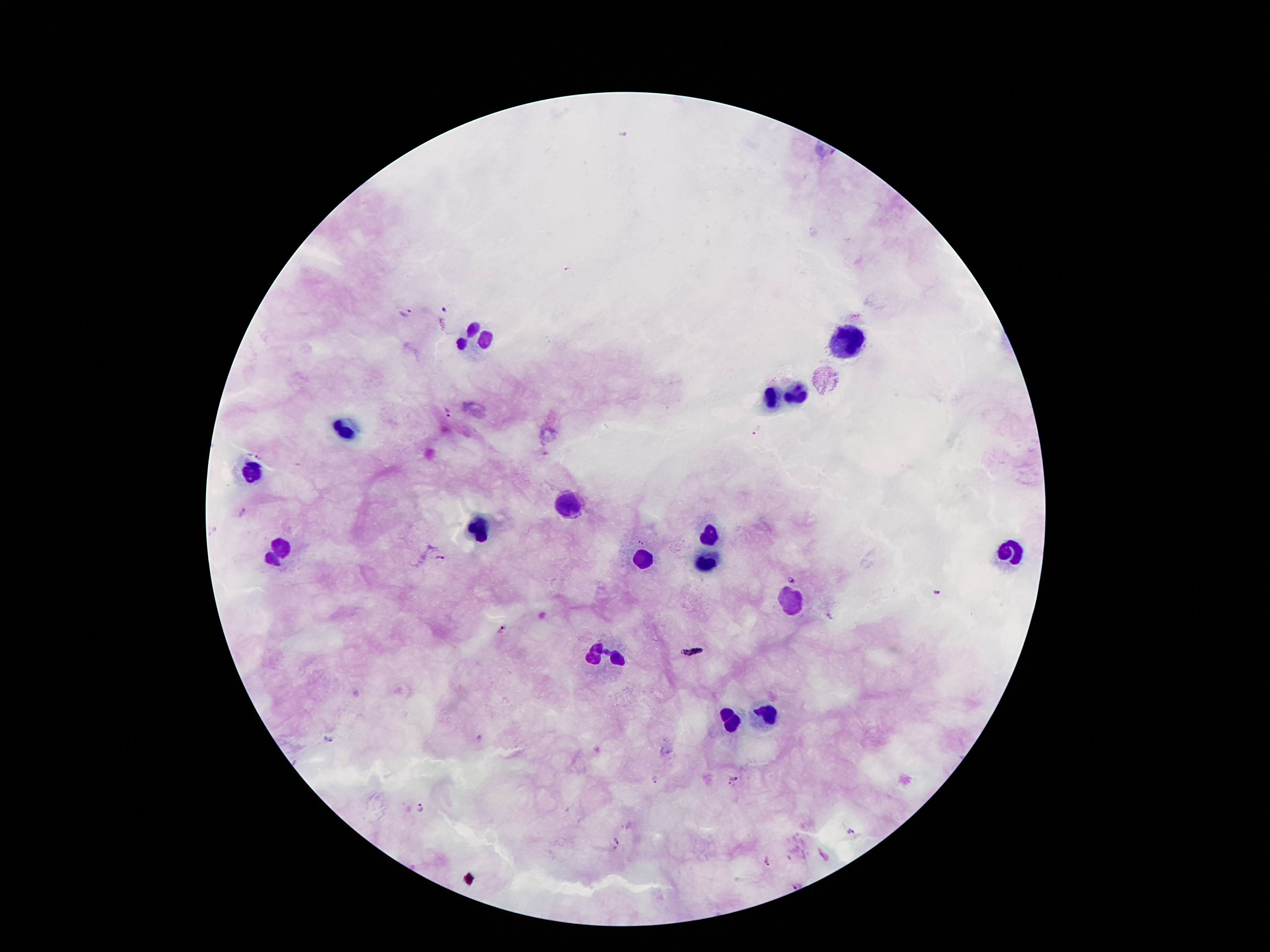
Approximate object centers, in pixels from the top-left corner.
Summary:
  - Plasmodium parasite locations: (x=625, y=135), (x=446, y=309), (x=405, y=313), (x=447, y=414), (x=759, y=430), (x=258, y=458), (x=241, y=511), (x=440, y=557), (x=791, y=579), (x=936, y=592), (x=500, y=631), (x=328, y=740), (x=655, y=780), (x=733, y=782), (x=423, y=805), (x=850, y=831), (x=615, y=843), (x=766, y=861), (x=797, y=885)
  - Leukocyte locations: (x=473, y=336), (x=843, y=343), (x=770, y=396), (x=798, y=398), (x=347, y=428), (x=251, y=474), (x=572, y=507), (x=483, y=528), (x=711, y=538), (x=276, y=552), (x=1007, y=554), (x=704, y=557), (x=641, y=559), (x=790, y=602), (x=606, y=655), (x=768, y=714), (x=731, y=721)
  - Capture: smartphone camera through the microscope eyepiece
  - Preparation: thick peripheral-blood smear
  - Image size: 1270×952 pixels
  - Magnification: 100x
  - Patient malaria status: positive for Plasmodium falciparum
  - Stain: Giemsa
  - Field of view: one from this slide